Outline platelets.
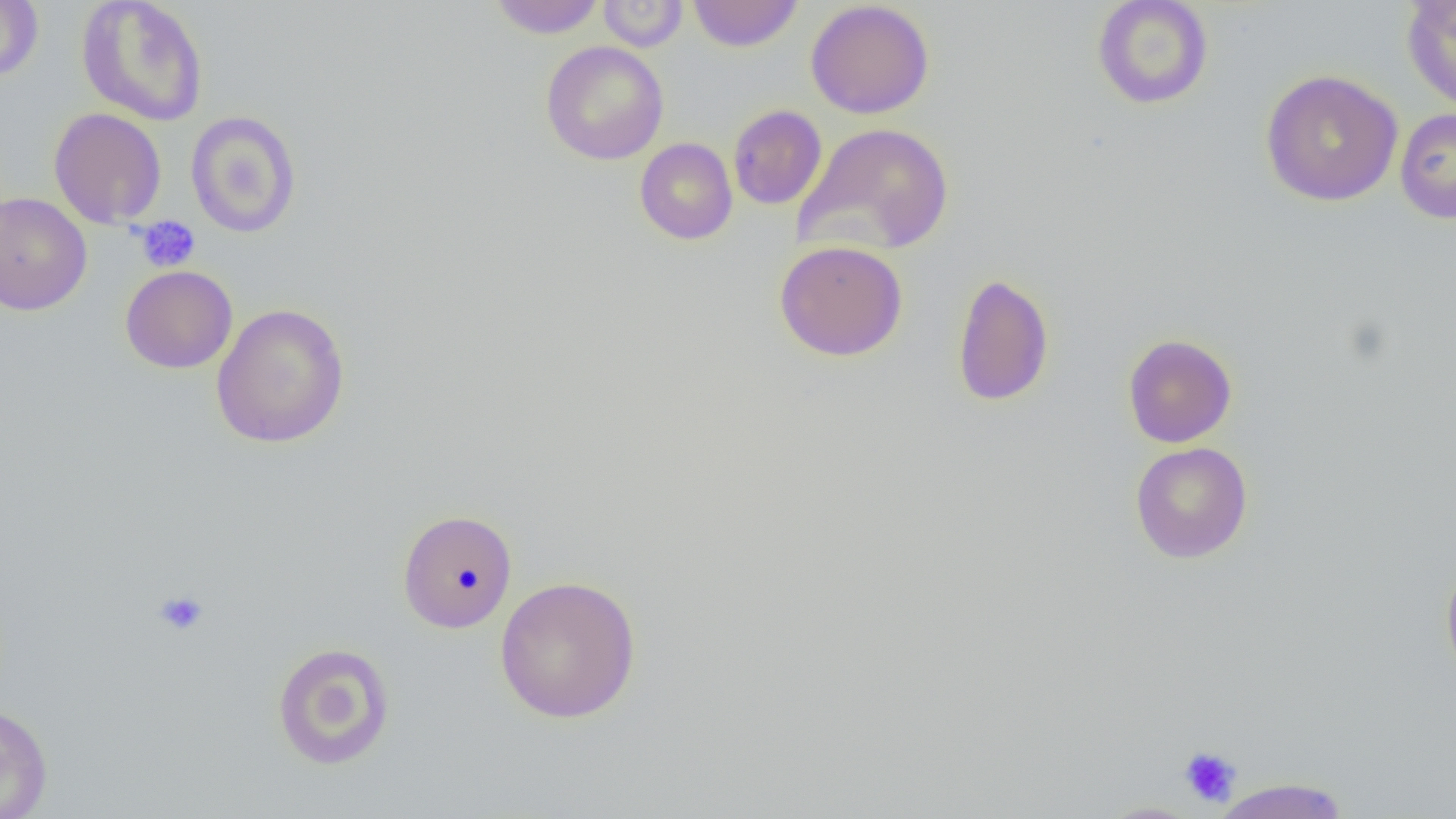
Approximate bounding boxes as named x1/y1/x2/y2 corners in pixels.
Platelets: (x1=134, y1=216, x2=200, y2=272), (x1=153, y1=589, x2=209, y2=636), (x1=1178, y1=745, x2=1242, y2=807).

Uninfected red blood cell locations: (x1=487, y1=0, x2=607, y2=38), (x1=597, y1=0, x2=688, y2=52), (x1=687, y1=0, x2=803, y2=52), (x1=1091, y1=0, x2=1214, y2=110), (x1=1401, y1=0, x2=1456, y2=113), (x1=0, y1=1, x2=43, y2=82), (x1=76, y1=1, x2=209, y2=127), (x1=805, y1=1, x2=935, y2=119), (x1=540, y1=40, x2=669, y2=165), (x1=1260, y1=69, x2=1403, y2=206), (x1=728, y1=105, x2=827, y2=210), (x1=49, y1=107, x2=166, y2=228), (x1=1395, y1=107, x2=1456, y2=223), (x1=185, y1=110, x2=302, y2=238), (x1=794, y1=121, x2=955, y2=257), (x1=634, y1=138, x2=738, y2=245), (x1=0, y1=191, x2=92, y2=316), (x1=774, y1=240, x2=908, y2=361), (x1=120, y1=265, x2=238, y2=374), (x1=952, y1=271, x2=1055, y2=407), (x1=211, y1=302, x2=350, y2=450), (x1=1123, y1=333, x2=1237, y2=448), (x1=1130, y1=442, x2=1253, y2=563), (x1=397, y1=509, x2=518, y2=634), (x1=1440, y1=557, x2=1456, y2=686), (x1=494, y1=575, x2=641, y2=724), (x1=271, y1=641, x2=396, y2=770), (x1=0, y1=703, x2=53, y2=818), (x1=1208, y1=777, x2=1353, y2=819), (x1=1097, y1=801, x2=1205, y2=819). Slide-level diagnosis: no evidence of blood parasites. Image is 1456×819 pixels. One field of a larger specimen. Light microscopy. Thin blood film. 1000x magnification.